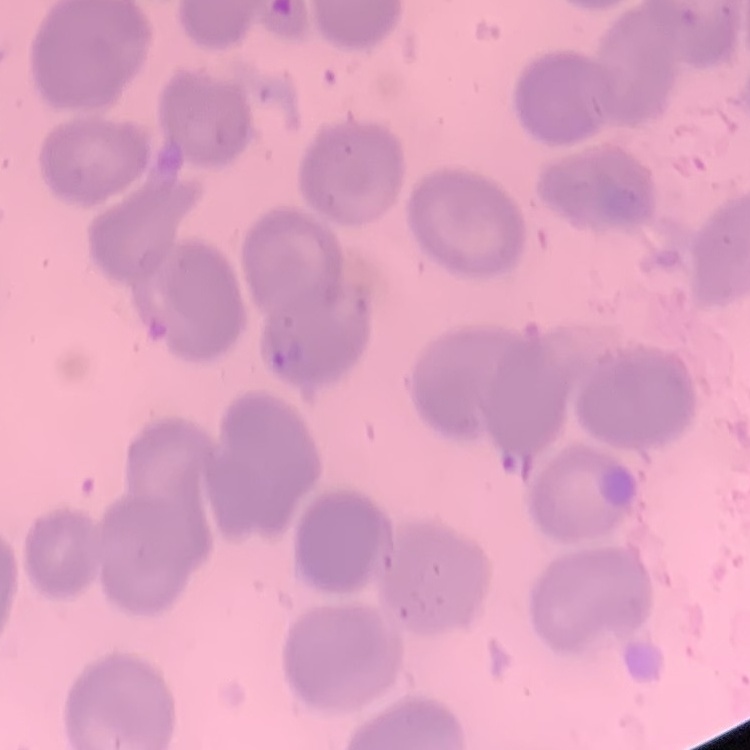

The red blood cells exhibit no rouleaux formation. Thin peripheral smear. Field's or Giemsa stain. One tile cut from a larger photomicrograph.